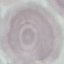
Summary:
  - Result: no malaria parasites detected
  - Capture: smartphone camera at the microscope eyepiece
  - Image type: cell patch, automatically extracted from a larger field of view and resized to 64 × 64 pixels
  - Preparation: thin smear
  - Stain: Giemsa